Comment on the morphology of the erythrocytes.
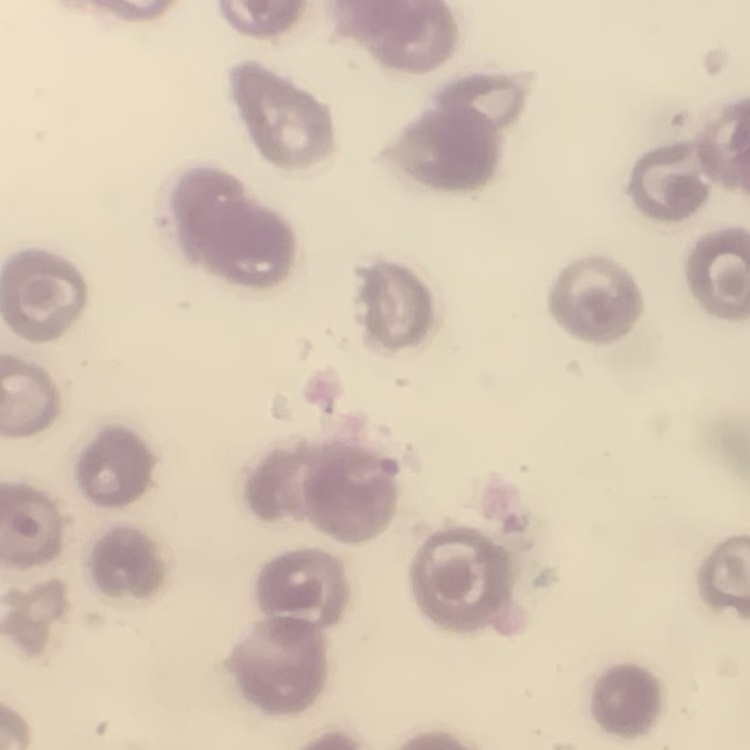

They show no rouleaux formation.

Thin blood smear. One tile cut from a larger photomicrograph. Stained with either Field's or Giemsa.